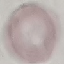
Result: no malaria parasites detected. Giemsa stain. Thin blood film. Acquired by smartphone through the microscope eyepiece. Automatically extracted cell patch, resized to 64 × 64 pixels.